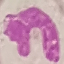
{
  "result": "no malaria parasites detected",
  "preparation": "thin smear",
  "image_type": "cell patch, automatically extracted from a larger field of view and resized to 64 × 64 pixels",
  "stain": "Giemsa",
  "capture": "smartphone camera at the microscope eyepiece"
}